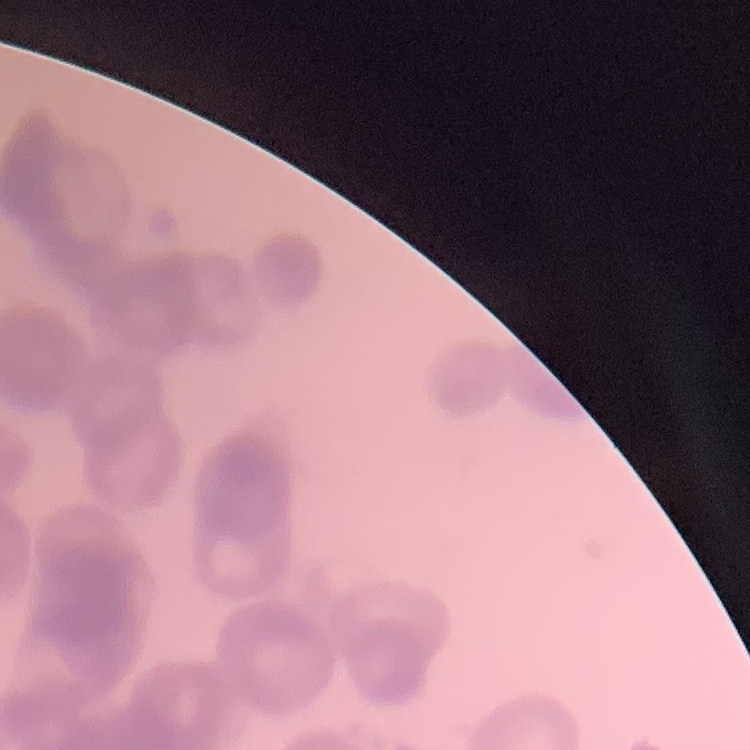 The erythrocytes show rouleaux formation. Square crop of a larger photomicrograph. Thin peripheral smear. Stained with either Field's or Giemsa.